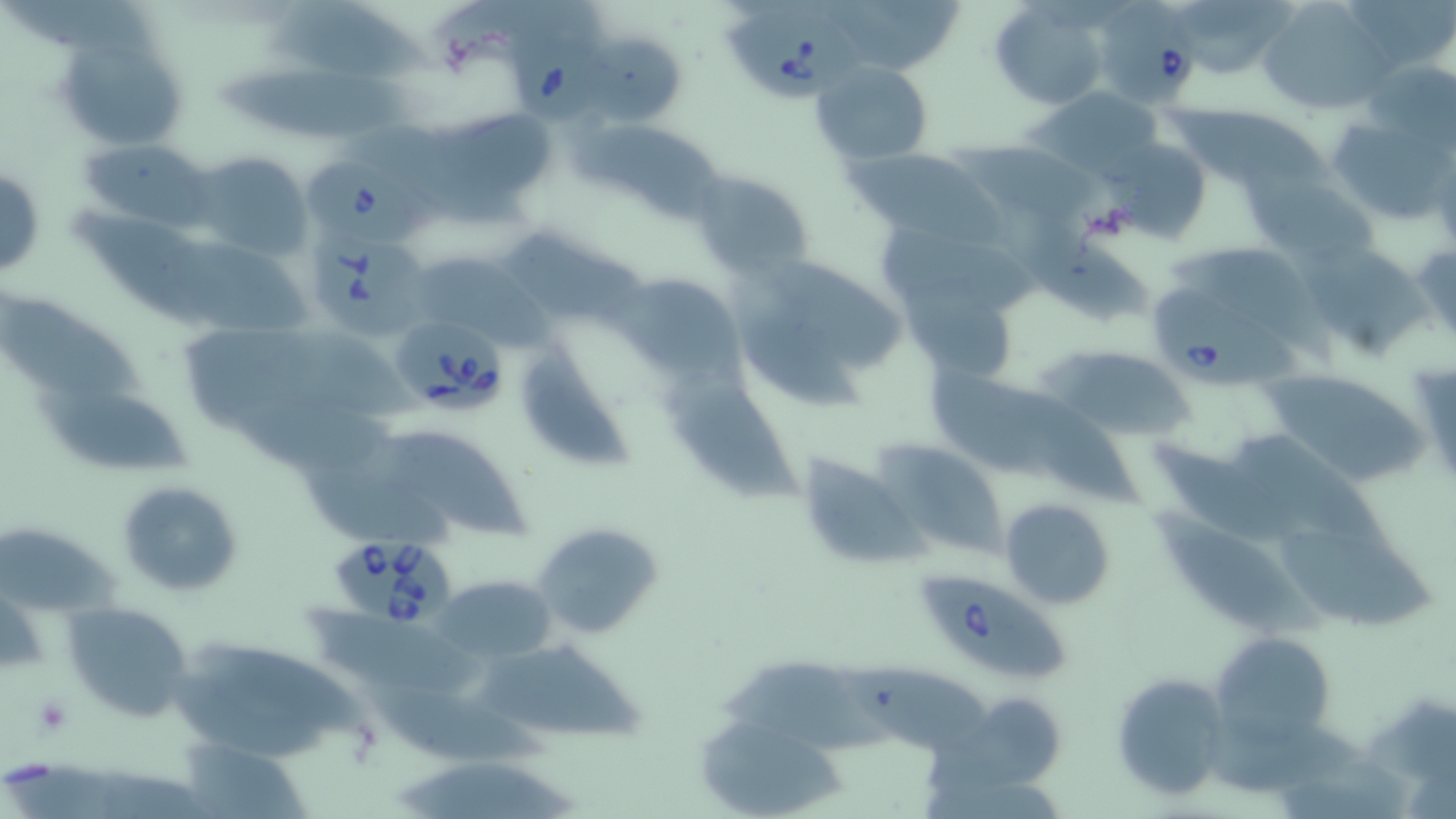
slide-level diagnosis = Babesia divergens
preparation = thin blood smear
stain = May-Grünwald-Giemsa
field of view = one of a larger specimen
uninfected red blood cell locations = approximate bounding boxes as (x1,y1)-(x2,y2) corner pairs in pixels: (266,0)-(434,84), (821,0)-(964,72), (1182,0)-(1304,72), (988,1)-(1108,110), (1258,1)-(1390,117), (51,22)-(193,155), (579,33)-(688,127), (1366,59)-(1453,149), (810,60)-(933,164), (217,66)-(416,136), (1026,86)-(1168,181), (1173,104)-(1328,192), (1322,113)-(1454,223), (581,130)-(736,231), (79,138)-(214,229), (955,139)-(1104,221), (1107,139)-(1211,246), (850,147)-(991,238), (188,152)-(311,260), (0,170)-(46,276), (690,172)-(815,283), (1250,173)-(1376,265), (998,203)-(1159,329), (67,204)-(219,333), (505,231)-(660,325), (1302,241)-(1433,363), (1174,245)-(1326,352), (405,250)-(531,347), (767,259)-(901,368), (617,272)-(741,386), (904,274)-(1011,381), (1,290)-(149,396), (738,305)-(864,414), (520,340)-(635,474), (1052,347)-(1193,443), (930,363)-(1050,484), (1261,366)-(1428,485), (661,377)-(806,504), (28,387)-(207,476), (1001,390)-(1150,513), (1244,429)-(1399,553), (372,431)-(536,543), (878,441)-(1003,558), (1158,442)-(1302,549), (795,454)-(923,568), (297,467)-(467,551), (116,480)-(243,597), (1001,497)-(1115,608), (1157,509)-(1325,636), (533,521)-(664,639), (0,527)-(124,616), (1278,528)-(1440,636), (431,573)-(557,663), (63,601)-(194,722), (309,612)-(496,700), (1211,633)-(1335,741), (192,640)-(370,737), (477,651)-(647,744), (722,660)-(893,754), (843,660)-(996,750), (1110,672)-(1232,803), (360,681)-(560,771), (921,698)-(1066,804), (1364,700)-(1456,779), (695,712)-(847,818), (1211,717)-(1369,791), (182,737)-(307,816), (397,759)-(584,819)
magnification = 1000x
modality = optical microscopy
platelet locations = approximate bounding boxes as (x1,y1)-(x2,y2) corner pairs in pixels: (33,695)-(72,738)
image size = 1456×819 pixels
Babesia divergens-infected red blood cell locations = approximate bounding boxes as (x1,y1)-(x2,y2) corner pairs in pixels: (1102,0)-(1202,109), (503,8)-(612,132), (720,9)-(868,103), (303,158)-(436,246), (313,231)-(419,344), (1151,284)-(1315,388), (391,315)-(509,416), (327,533)-(457,626), (919,566)-(1065,679)